Identify the blood parasite species.
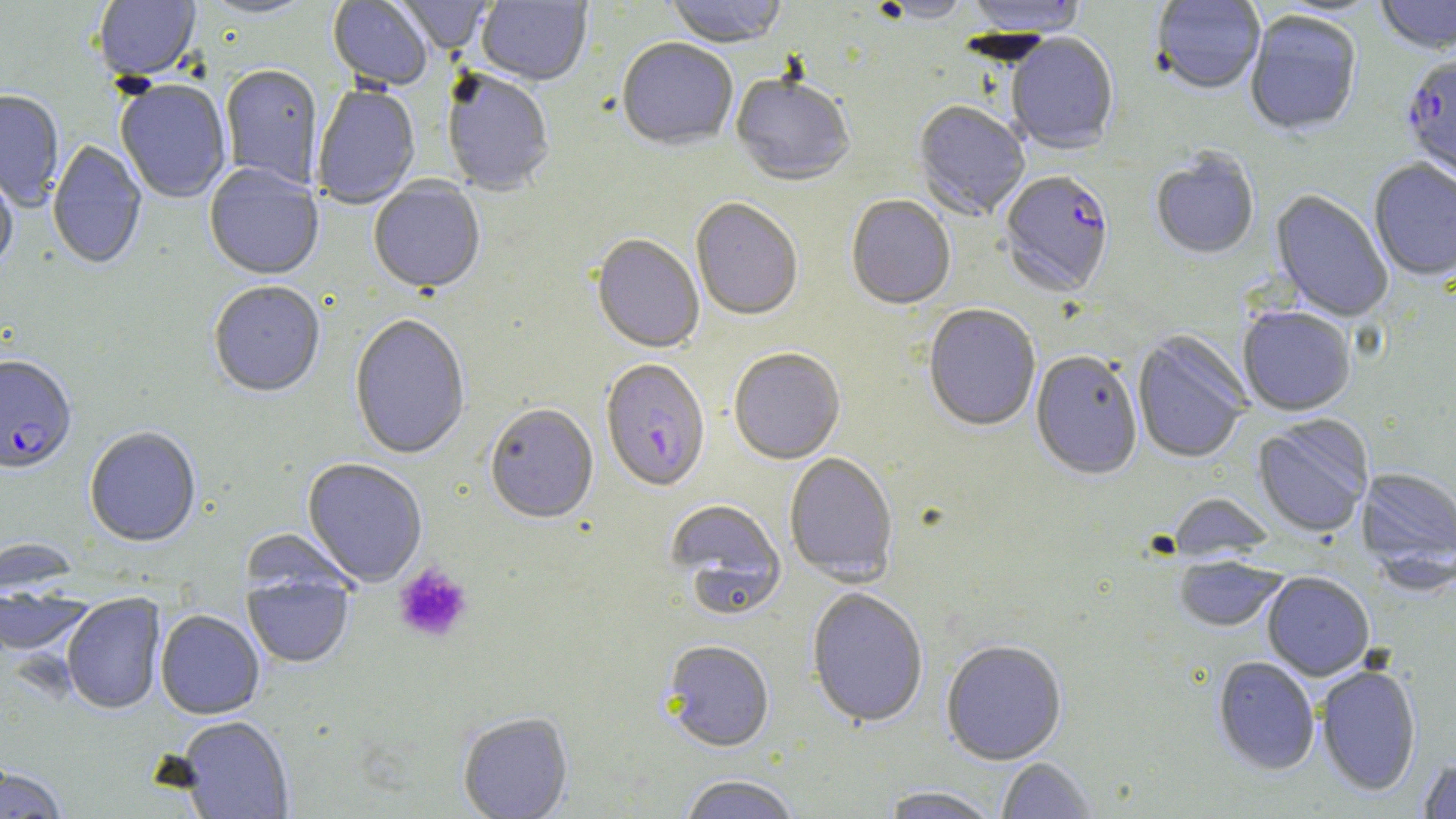

Plasmodium falciparum.

magnification: 1000x
plasmodium_falciparum_infected_red_blood_cell_locations: 'approximate bounding boxes as named x1/y1/x2/y2 corners in pixels: (x1=1401, y1=55, x2=1456, y2=188), (x1=999, y1=172, x2=1114, y2=299), (x1=0, y1=357, x2=77, y2=476), (x1=602, y1=365, x2=711, y2=498)'
image_size: 1456×819 pixels
modality: optical microscopy
field_of_view: single
preparation: thin blood film
uninfected_red_blood_cell_locations: 'approximate bounding boxes as named x1/y1/x2/y2 corners in pixels: (x1=197, y1=0, x2=319, y2=21), (x1=328, y1=0, x2=432, y2=92), (x1=393, y1=0, x2=493, y2=57), (x1=476, y1=0, x2=593, y2=88), (x1=664, y1=0, x2=787, y2=51), (x1=965, y1=0, x2=1087, y2=40), (x1=1150, y1=0, x2=1266, y2=96), (x1=1375, y1=0, x2=1456, y2=57), (x1=92, y1=1, x2=200, y2=83), (x1=872, y1=1, x2=974, y2=25), (x1=1245, y1=13, x2=1361, y2=138), (x1=1006, y1=34, x2=1119, y2=156), (x1=616, y1=39, x2=738, y2=153), (x1=220, y1=66, x2=323, y2=190), (x1=441, y1=72, x2=555, y2=197), (x1=731, y1=76, x2=854, y2=188), (x1=116, y1=81, x2=232, y2=204), (x1=313, y1=85, x2=420, y2=210), (x1=0, y1=91, x2=64, y2=211), (x1=913, y1=101, x2=1030, y2=221), (x1=46, y1=139, x2=147, y2=272), (x1=1151, y1=152, x2=1259, y2=261), (x1=1368, y1=160, x2=1456, y2=282), (x1=0, y1=165, x2=18, y2=276), (x1=204, y1=165, x2=324, y2=282), (x1=368, y1=180, x2=485, y2=297), (x1=1270, y1=191, x2=1393, y2=323), (x1=846, y1=196, x2=956, y2=311), (x1=691, y1=199, x2=803, y2=322), (x1=591, y1=236, x2=704, y2=355), (x1=208, y1=283, x2=325, y2=399), (x1=923, y1=306, x2=1040, y2=433), (x1=1238, y1=308, x2=1355, y2=417), (x1=349, y1=315, x2=470, y2=461), (x1=1132, y1=332, x2=1251, y2=464), (x1=729, y1=349, x2=845, y2=465), (x1=1030, y1=352, x2=1142, y2=481), (x1=485, y1=405, x2=598, y2=525), (x1=1253, y1=416, x2=1373, y2=538), (x1=84, y1=428, x2=201, y2=547), (x1=784, y1=453, x2=898, y2=586), (x1=302, y1=459, x2=427, y2=587), (x1=1356, y1=466, x2=1456, y2=584), (x1=1167, y1=494, x2=1274, y2=562), (x1=665, y1=500, x2=786, y2=617), (x1=241, y1=530, x2=358, y2=600), (x1=1175, y1=556, x2=1286, y2=632), (x1=243, y1=573, x2=355, y2=669), (x1=1263, y1=573, x2=1375, y2=681), (x1=1, y1=584, x2=94, y2=659), (x1=806, y1=588, x2=929, y2=729), (x1=62, y1=594, x2=166, y2=716), (x1=155, y1=611, x2=264, y2=720), (x1=941, y1=641, x2=1067, y2=766), (x1=662, y1=642, x2=775, y2=754), (x1=1213, y1=657, x2=1320, y2=776), (x1=1315, y1=664, x2=1421, y2=797), (x1=458, y1=713, x2=573, y2=819), (x1=176, y1=717, x2=295, y2=818), (x1=1418, y1=756, x2=1456, y2=818), (x1=997, y1=758, x2=1096, y2=818), (x1=0, y1=767, x2=69, y2=818), (x1=680, y1=776, x2=800, y2=819), (x1=878, y1=787, x2=1002, y2=819)'
stain: May-Grünwald-Giemsa
platelet_locations: 'approximate bounding boxes as named x1/y1/x2/y2 corners in pixels: (x1=393, y1=563, x2=473, y2=643)'